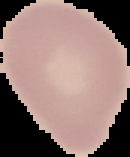

image_size: 130×157 pixels
image_type: segmented cell region on a black background
result: no Plasmodium parasites detected
preparation: thin blood smear